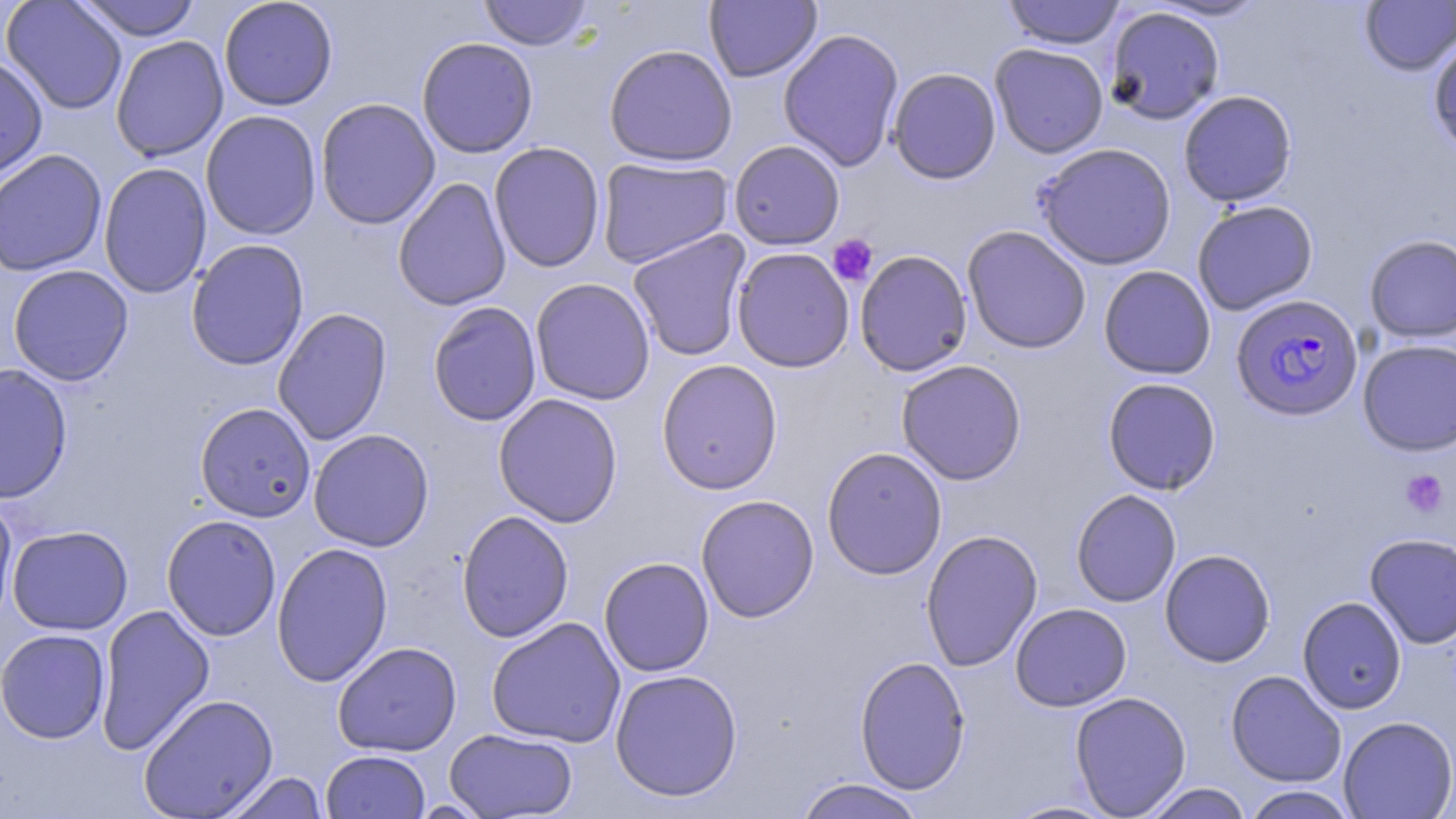
slide-level diagnosis = Plasmodium falciparum
platelet locations = approximate bounding boxes as (x1,y1)-(x2,y2) corner pairs in pixels: (828,234)-(878,287), (1400,470)-(1449,517)
preparation = thin blood smear
stain = May-Grünwald-Giemsa
Plasmodium falciparum-infected red blood cell locations = approximate bounding boxes as (x1,y1)-(x2,y2) corner pairs in pixels: (1231,294)-(1364,420)
image size = 1456×819 pixels
modality = light microscopy
magnification = 1000x
field of view = single
uninfected red blood cell locations = approximate bounding boxes as (x1,y1)-(x2,y2) corner pairs in pixels: (1,0)-(128,115), (73,0)-(202,41), (218,0)-(338,111), (478,0)-(594,50), (704,0)-(822,83), (1001,0)-(1126,50), (1148,0)-(1270,22), (1359,0)-(1456,76), (1106,6)-(1225,125), (778,28)-(905,172), (1428,31)-(1456,158), (110,35)-(229,162), (416,37)-(539,159), (604,43)-(738,167), (989,43)-(1109,159), (0,55)-(49,185), (887,67)-(1001,184), (1178,90)-(1298,207), (315,97)-(441,230), (200,109)-(322,240), (728,140)-(845,250), (489,142)-(606,273), (1035,142)-(1177,270), (0,149)-(107,277), (596,157)-(734,269), (98,162)-(212,299), (392,177)-(512,311), (1191,200)-(1318,315), (961,225)-(1092,354), (627,229)-(752,362), (1364,234)-(1456,343), (186,239)-(309,371), (731,247)-(855,373), (854,249)-(973,377), (8,264)-(134,386), (1099,265)-(1216,379), (530,277)-(656,405), (427,301)-(542,427), (272,307)-(393,446), (1357,339)-(1456,455), (656,359)-(783,495), (896,359)-(1027,485), (0,362)-(73,504), (1102,377)-(1221,495), (493,393)-(624,528), (195,402)-(316,522), (308,429)-(435,552), (821,446)-(948,580), (1071,489)-(1181,607), (0,493)-(19,632), (695,494)-(820,622), (456,510)-(574,643), (161,514)-(282,641), (7,525)-(133,635), (920,529)-(1043,672), (1364,532)-(1456,649), (271,541)-(394,687), (1159,549)-(1276,667), (598,556)-(714,677), (1297,596)-(1407,714), (1010,603)-(1132,711), (95,604)-(215,756), (486,616)-(626,748), (0,628)-(111,743), (332,641)-(462,757), (854,655)-(971,794), (609,668)-(743,802), (1225,670)-(1346,787), (1070,691)-(1191,818), (138,693)-(279,819), (1338,716)-(1456,818), (444,728)-(578,818), (321,750)-(430,819), (218,771)-(328,819), (793,778)-(928,819), (1138,782)-(1253,819), (1241,787)-(1357,819), (1002,799)-(1120,818)